Give the position of every Plasmodium falciparum parasite, noting its life-cycle stage.
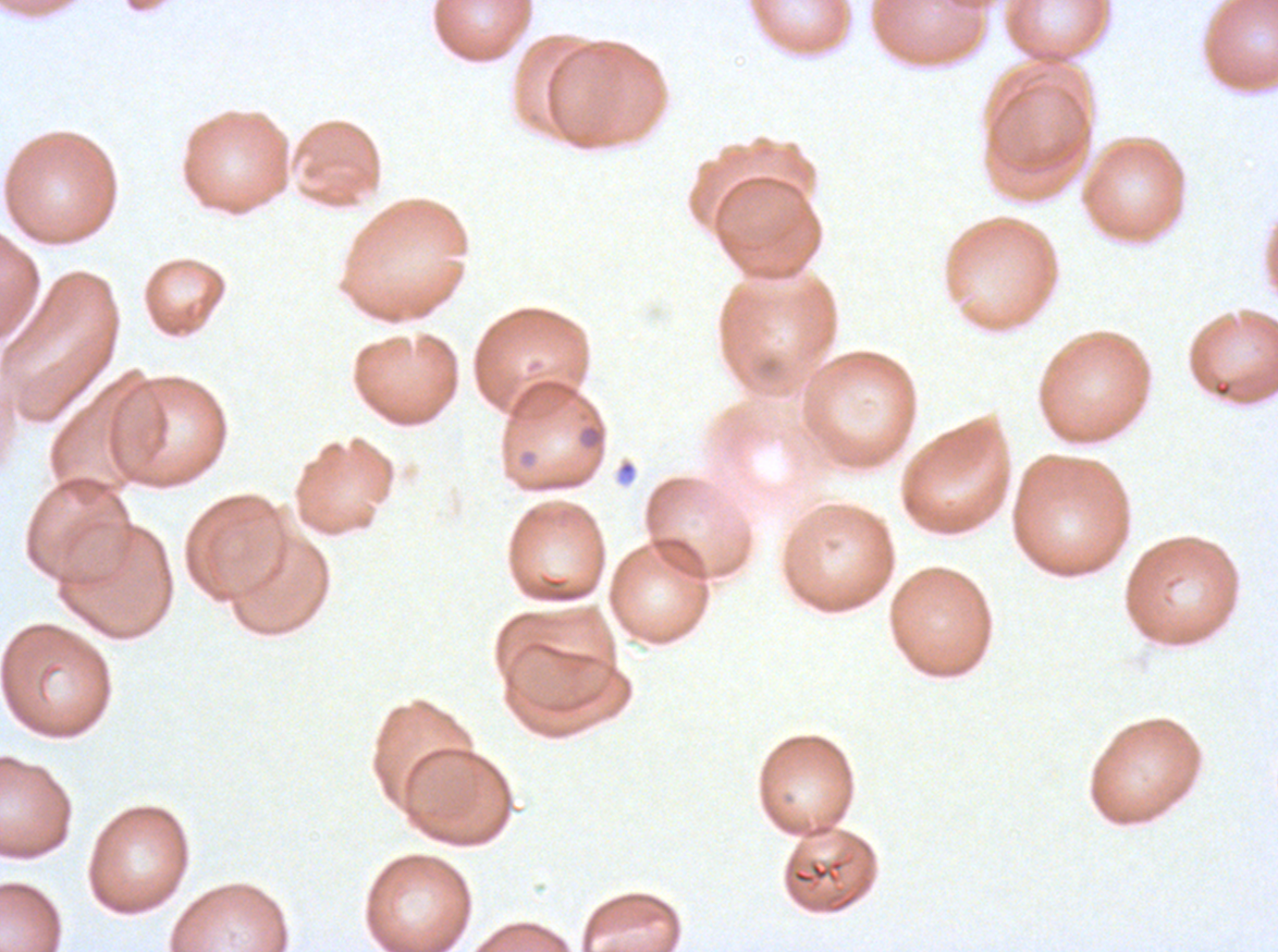
No rings, late-ring/early-trophozoite forms, mid trophozoites, late trophozoites, early schizonts, late schizonts, segmenters, or gametocytes observed.

stain: Giemsa
field_of_view: sub-image separated from a larger composite
image_size: 1278×952 pixels
specimen: ex-vivo Plasmodium falciparum culture from a patient in The Gambia, grown for 24 to 48 hours
debris_locations: 'approximate bounding boxes as [x1, y1, x2, y2] in pixels: [584, 424, 603, 449], [786, 857, 846, 890]'
preparation: thin blood film